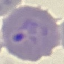 Result: malaria parasites identified. Cell patch, automatically extracted from a larger field of view and resized to 64 × 64 pixels. Giemsa stain. Acquired by smartphone through the microscope eyepiece. Thin blood film.